Outline each Plasmodium vivax-infected red blood cell.
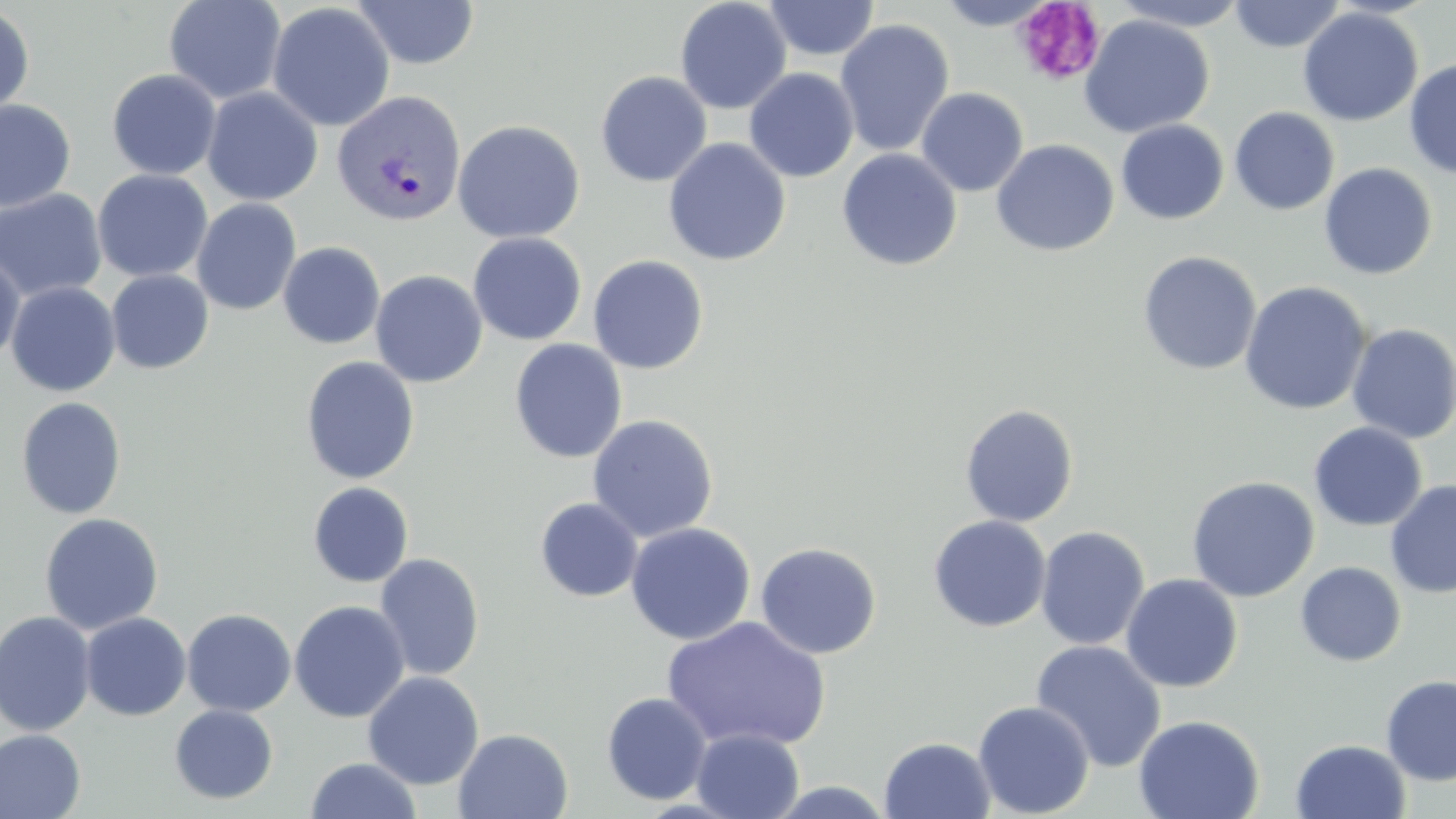

Approximate bounding boxes as (x1, y1, x2, y2) in pixels.
Plasmodium vivax-infected red blood cells: (332, 89, 467, 228).

slide-level diagnosis = Plasmodium vivax
magnification = 1000x
modality = light microscopy
field of view = single
platelet locations = approximate bounding boxes as (x1, y1, x2, y2) in pixels: (1013, 1, 1107, 87)
preparation = thin blood smear
image size = 1456×819 pixels
uninfected red blood cell locations = approximate bounding boxes as (x1, y1, x2, y2) in pixels: (163, 0, 287, 104), (351, 0, 481, 69), (675, 0, 792, 115), (764, 0, 880, 61), (1110, 0, 1253, 31), (935, 1, 1056, 30), (1228, 1, 1347, 53), (267, 2, 395, 132), (0, 5, 35, 121), (1297, 7, 1423, 126), (1079, 14, 1214, 138), (834, 19, 955, 157), (1404, 59, 1456, 179), (744, 68, 859, 182), (106, 69, 221, 180), (595, 71, 712, 187), (201, 87, 323, 206), (915, 87, 1029, 196), (0, 99, 76, 212), (1229, 107, 1340, 215), (452, 119, 585, 244), (1116, 119, 1229, 224), (663, 138, 791, 266), (991, 139, 1119, 256), (837, 148, 962, 272), (1318, 163, 1437, 280), (92, 169, 213, 282), (0, 188, 108, 303), (191, 198, 302, 316), (467, 232, 587, 345), (278, 241, 386, 350), (0, 251, 25, 367), (1137, 251, 1262, 375), (587, 255, 709, 374), (105, 269, 214, 374), (370, 269, 487, 388), (5, 281, 120, 397), (1239, 281, 1373, 416), (1347, 323, 1456, 444), (509, 339, 627, 463), (300, 356, 420, 485), (16, 396, 127, 519), (960, 403, 1079, 526), (587, 414, 719, 542), (1309, 422, 1428, 532), (1186, 476, 1320, 602), (1385, 480, 1456, 598), (307, 481, 414, 587), (534, 497, 643, 602), (39, 513, 164, 635), (928, 515, 1052, 632), (625, 522, 756, 645), (1035, 525, 1150, 650), (755, 541, 882, 660), (374, 552, 485, 681), (1295, 561, 1407, 667), (1120, 573, 1243, 693), (288, 600, 410, 723), (181, 608, 297, 716), (0, 610, 97, 737), (80, 612, 191, 721), (662, 616, 831, 752), (1030, 639, 1167, 772), (363, 671, 484, 789), (1380, 675, 1456, 786), (601, 691, 713, 805), (973, 700, 1095, 818), (169, 704, 278, 804), (1133, 714, 1264, 819), (453, 728, 574, 819), (691, 728, 805, 819), (0, 729, 86, 819), (879, 736, 996, 819), (1290, 739, 1412, 819), (305, 757, 422, 818)
stain = May-Grünwald-Giemsa